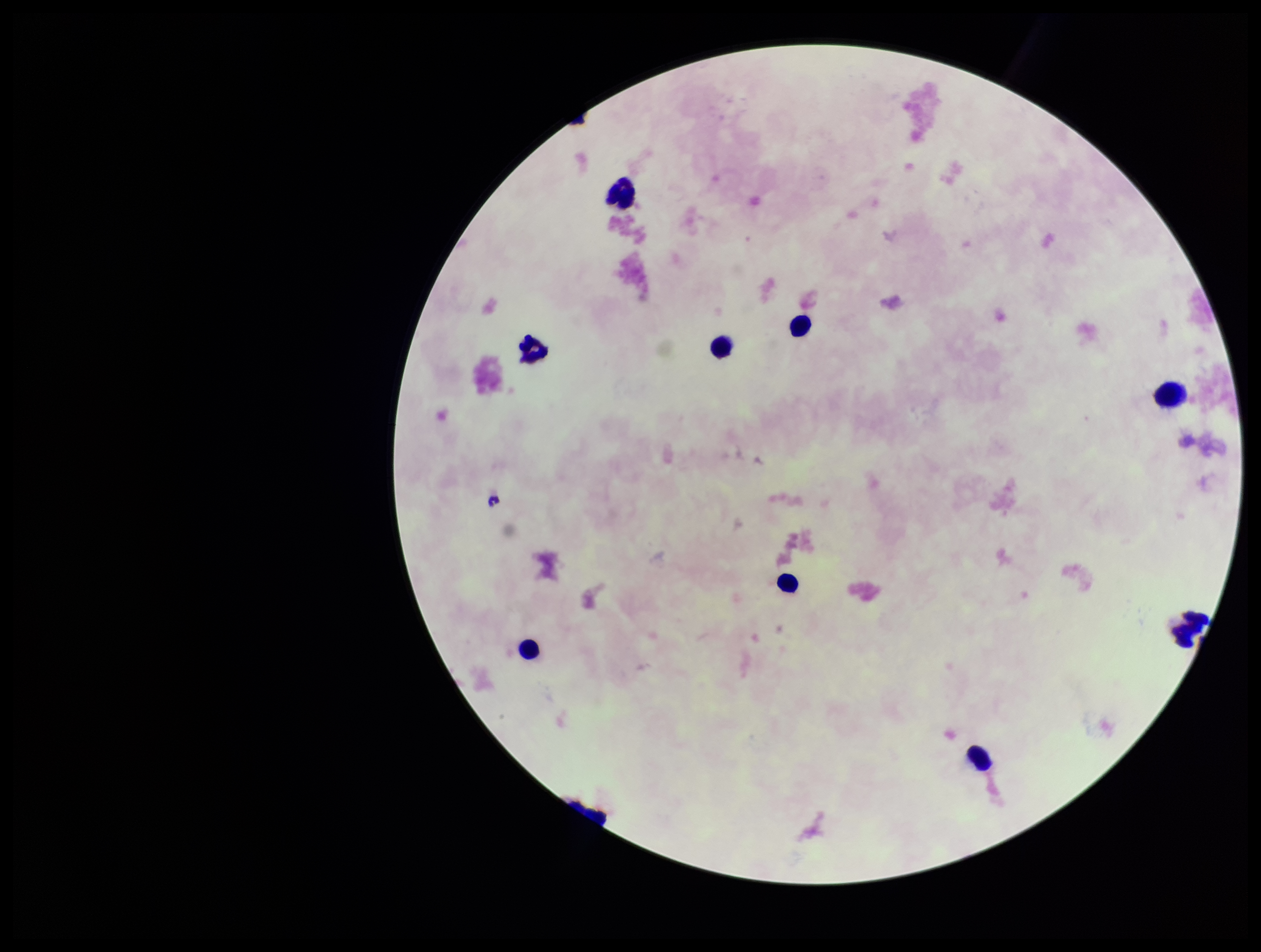
Parasite count: 0. Preparation: thick smear. Stained with Giemsa. Patient malaria status: negative. Image is 1261×952 pixels. Plasmodium parasites: none identified. Photographed through the microscope eyepiece with a smartphone camera. Leukocyte count: 9. Single field of view.